Locate every blood parasite and identify its species.
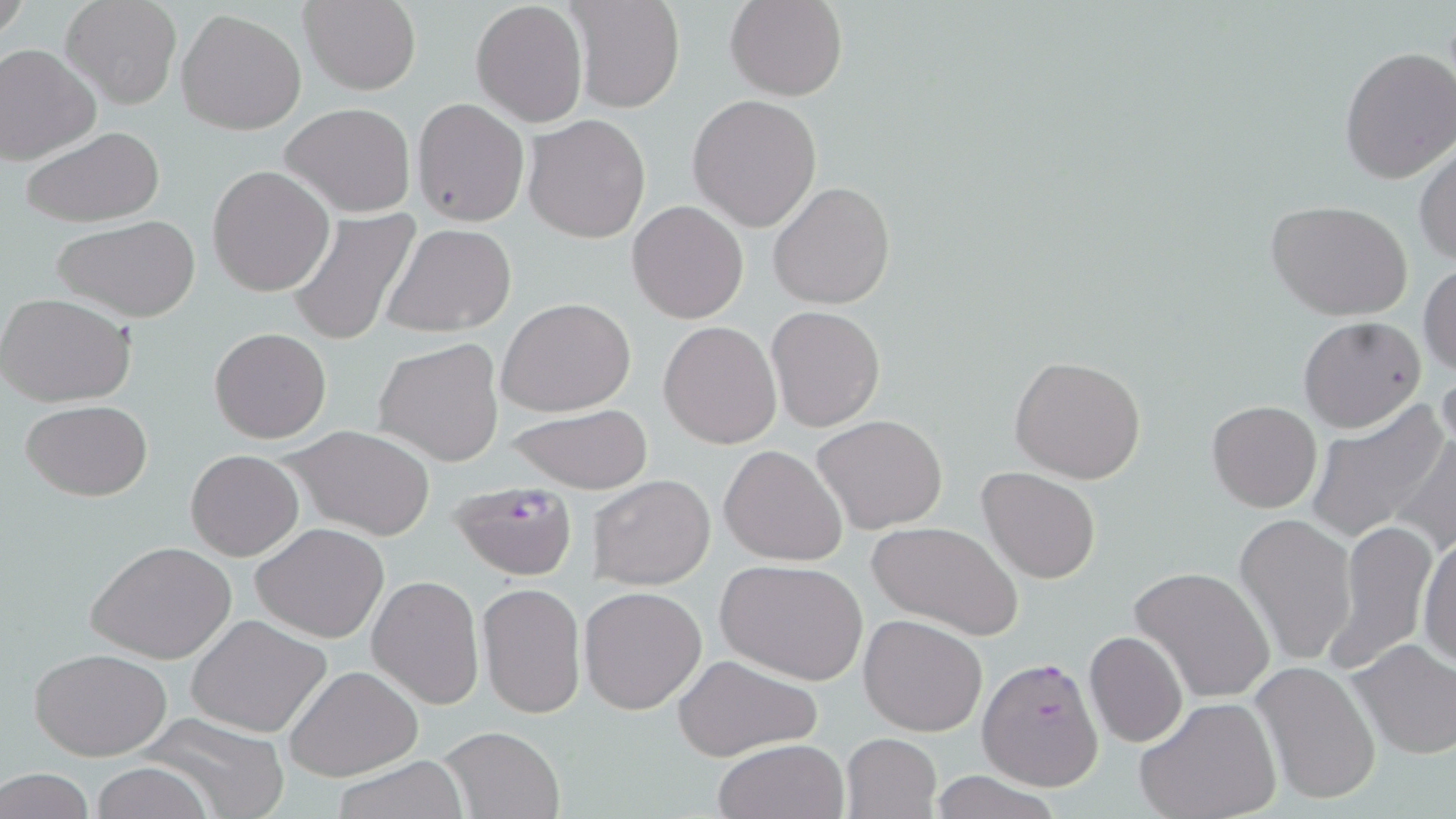

Approximate bounding boxes as (x1,y1)-(x2,y2) corner pairs in pixels.
Plasmodium falciparum-infected red blood cells: (449,478)-(580,582), (978,656)-(1104,790).
No Plasmodium ovale, Plasmodium malariae, Plasmodium vivax, Babesia divergens, or Trypanosoma brucei observed.

Uninfected red blood cell locations: (60,0)-(183,110), (569,0)-(683,113), (725,0)-(848,100), (300,1)-(421,95), (471,1)-(589,128), (177,10)-(307,135), (0,44)-(101,164), (1338,45)-(1456,185), (687,95)-(822,232), (411,98)-(529,228), (282,102)-(417,217), (522,113)-(652,245), (18,127)-(166,226), (1414,141)-(1456,267), (208,165)-(334,296), (767,181)-(895,311), (627,199)-(749,323), (1266,200)-(1414,321), (284,206)-(422,347), (52,215)-(199,322), (380,223)-(517,337), (1419,262)-(1455,377), (0,291)-(137,408), (496,297)-(636,417), (767,306)-(885,432), (1298,316)-(1425,432), (658,321)-(781,448), (208,327)-(331,445), (375,337)-(505,468), (1009,355)-(1149,484), (1434,362)-(1456,463), (20,399)-(153,500), (1207,400)-(1322,513), (1303,402)-(1450,543), (503,404)-(654,494), (812,415)-(949,535), (279,425)-(437,540), (1391,428)-(1456,558), (720,444)-(849,566), (186,450)-(305,560), (977,467)-(1100,584), (586,474)-(716,591), (1234,513)-(1357,667), (1330,520)-(1436,672), (868,521)-(1024,640), (251,523)-(389,642), (1417,528)-(1455,671), (89,540)-(237,664), (716,559)-(869,686), (1129,565)-(1276,703), (367,575)-(485,709), (477,582)-(585,718), (578,586)-(707,713), (859,613)-(986,736), (186,614)-(334,737), (1084,630)-(1187,748), (1349,639)-(1456,759), (27,647)-(174,761), (671,654)-(821,760), (1252,661)-(1380,805), (284,664)-(424,781), (1134,698)-(1281,819), (133,709)-(289,819), (436,724)-(566,818), (841,732)-(942,818), (713,739)-(848,819), (328,757)-(471,819), (88,762)-(218,819), (0,768)-(97,819). Slide-level diagnosis: Plasmodium falciparum. Thin blood smear. Light microscopy. Captured at 1000x magnification. Image is 1456×819 pixels. Single field of view. May-Grünwald-Giemsa stain.